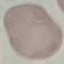

malaria status = uninfected
capture = smartphone camera at the microscope eyepiece
preparation = thin blood film
image type = automatically extracted cell patch, resized to 64 × 64 pixels
stain = Giemsa